Locate every blood parasite and identify its species.
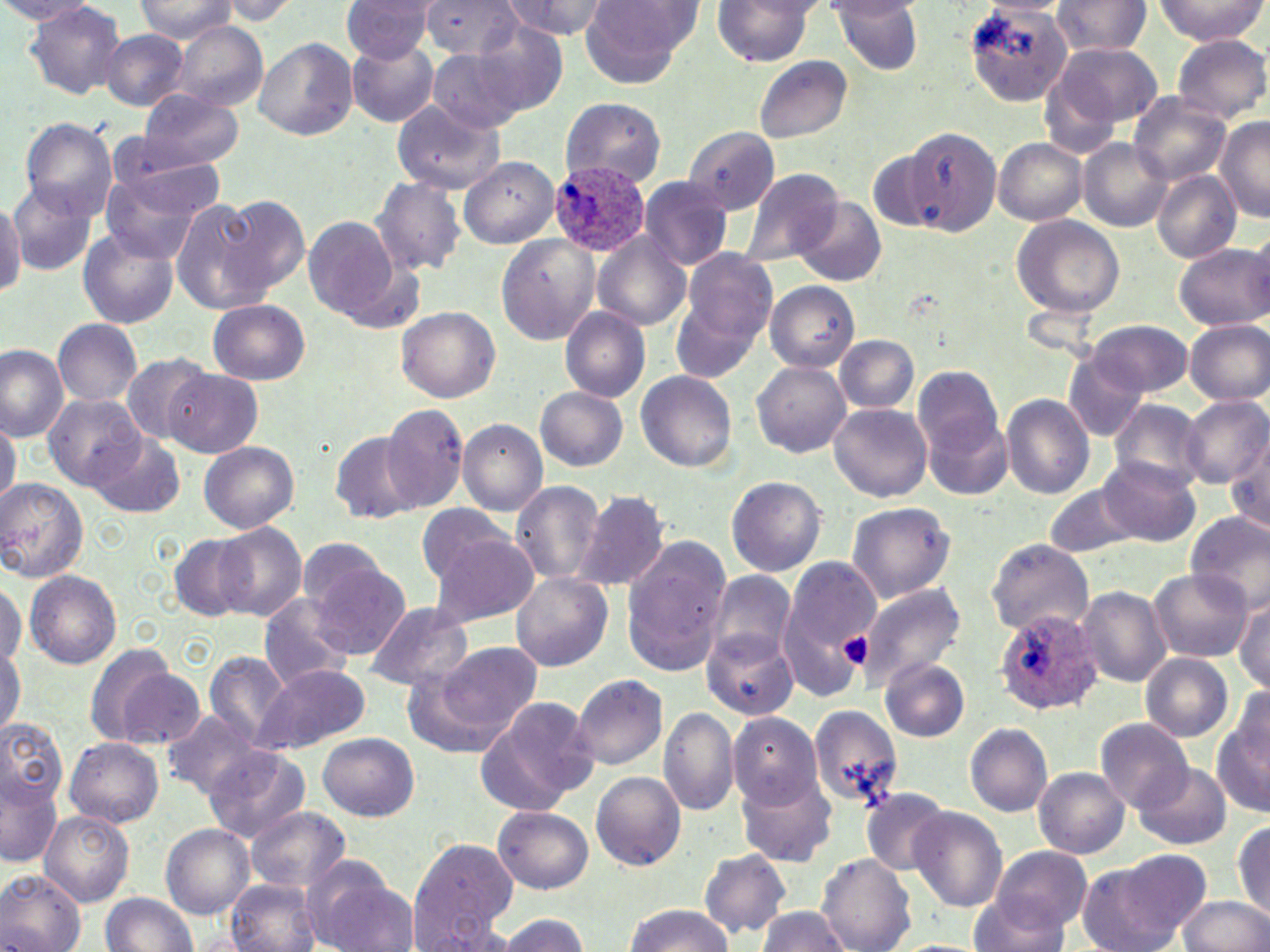

Approximate bounding boxes as (x1, y1, x2, y2) in pixels.
Plasmodium ovale-infected red blood cells: (550, 160, 651, 256), (993, 608, 1103, 717).
No Plasmodium falciparum, Plasmodium malariae, Plasmodium vivax, Babesia divergens, or Trypanosoma brucei observed.

Summary:
  - Uninfected red blood cell locations: (341, 0, 437, 63), (421, 0, 522, 61), (500, 0, 605, 44), (712, 0, 817, 66), (1050, 0, 1152, 60), (1153, 0, 1267, 44), (136, 1, 237, 42), (215, 1, 299, 24), (579, 1, 698, 87), (963, 1, 1076, 105), (978, 1, 1074, 19), (25, 2, 126, 101), (832, 2, 925, 75), (471, 21, 571, 116), (172, 22, 268, 110), (101, 30, 188, 110), (1172, 34, 1270, 123), (254, 37, 358, 140), (347, 40, 440, 127), (1051, 41, 1162, 127), (429, 49, 528, 134), (751, 55, 853, 144), (136, 92, 245, 168), (1128, 93, 1231, 185), (560, 97, 666, 189), (392, 100, 505, 194), (1215, 115, 1268, 223), (20, 118, 119, 217), (908, 126, 1003, 237), (684, 128, 782, 215), (107, 134, 230, 217), (994, 137, 1087, 225), (1078, 139, 1171, 230), (458, 156, 560, 249), (738, 168, 843, 269), (1151, 170, 1242, 261), (103, 172, 207, 265), (370, 174, 468, 276), (637, 177, 734, 271), (9, 181, 100, 275), (0, 194, 23, 298), (218, 194, 309, 293), (794, 197, 886, 286), (169, 199, 267, 314), (1011, 214, 1124, 318), (304, 217, 404, 321), (77, 230, 178, 329), (495, 234, 598, 344), (592, 234, 691, 331), (1174, 243, 1269, 330), (678, 248, 779, 355), (766, 281, 859, 371), (673, 288, 768, 381), (207, 299, 311, 385), (560, 306, 652, 402), (396, 308, 501, 402), (54, 318, 143, 406), (1087, 319, 1195, 396), (1184, 320, 1270, 406), (835, 334, 918, 413), (0, 344, 68, 441), (122, 352, 213, 447), (1060, 356, 1149, 442), (752, 359, 851, 457), (912, 366, 1002, 456), (165, 369, 263, 459), (635, 371, 736, 471), (535, 387, 629, 470), (41, 393, 145, 491), (1002, 394, 1096, 499), (1180, 396, 1270, 488), (1107, 401, 1208, 490), (829, 402, 933, 501), (380, 403, 470, 514), (925, 411, 1013, 500), (0, 417, 20, 507), (457, 420, 546, 516), (330, 433, 419, 525), (89, 434, 185, 519), (1227, 435, 1270, 539), (200, 441, 299, 532), (1102, 457, 1201, 547), (726, 476, 826, 577), (0, 478, 88, 582), (510, 480, 608, 584), (1041, 483, 1144, 558), (574, 489, 671, 591), (846, 502, 955, 603), (415, 506, 520, 586), (1184, 510, 1270, 613), (215, 522, 307, 620), (170, 533, 256, 623), (427, 534, 540, 627), (294, 538, 394, 624), (620, 538, 731, 677), (986, 539, 1092, 635), (778, 555, 880, 690), (311, 559, 410, 659), (1150, 568, 1252, 661), (25, 570, 121, 669), (706, 570, 796, 664), (512, 572, 612, 673), (0, 580, 26, 668), (858, 582, 967, 690), (1077, 586, 1171, 688), (1233, 595, 1268, 692), (258, 596, 355, 690), (363, 601, 472, 691), (700, 626, 798, 720), (435, 640, 541, 738), (0, 645, 22, 734), (204, 651, 289, 746), (1139, 653, 1234, 741), (880, 657, 971, 742), (104, 660, 207, 749), (253, 664, 370, 754), (571, 674, 668, 771), (1226, 686, 1269, 776), (482, 695, 599, 809), (808, 704, 905, 809), (659, 706, 739, 817), (161, 709, 264, 797), (1213, 710, 1270, 819), (727, 712, 823, 810), (0, 718, 67, 810), (1092, 718, 1194, 814), (964, 723, 1052, 817), (318, 733, 418, 819), (65, 738, 164, 827), (203, 746, 310, 844), (1132, 761, 1231, 851), (1034, 767, 1130, 860), (0, 772, 62, 866), (591, 772, 686, 871), (739, 775, 836, 867), (859, 789, 954, 875), (246, 806, 350, 894), (493, 806, 593, 893), (908, 806, 1006, 911), (40, 811, 134, 906), (1233, 819, 1270, 919), (161, 824, 254, 919), (408, 839, 517, 945), (992, 845, 1091, 935), (699, 850, 792, 940), (817, 853, 915, 952), (1075, 854, 1207, 952), (308, 861, 414, 952), (0, 871, 87, 952), (226, 880, 322, 952), (102, 893, 198, 951), (968, 893, 1070, 952), (1179, 896, 1270, 952), (623, 904, 732, 952), (756, 906, 849, 952), (498, 914, 592, 952), (888, 939, 990, 952)
  - Platelet locations: (839, 629, 873, 670)
  - Slide-level diagnosis: Plasmodium ovale
  - Stain: May-Grünwald-Giemsa
  - Preparation: thin blood film
  - Image size: 1270×952 pixels
  - Magnification: 1000x
  - Field of view: one of a larger specimen
  - Modality: light microscopy